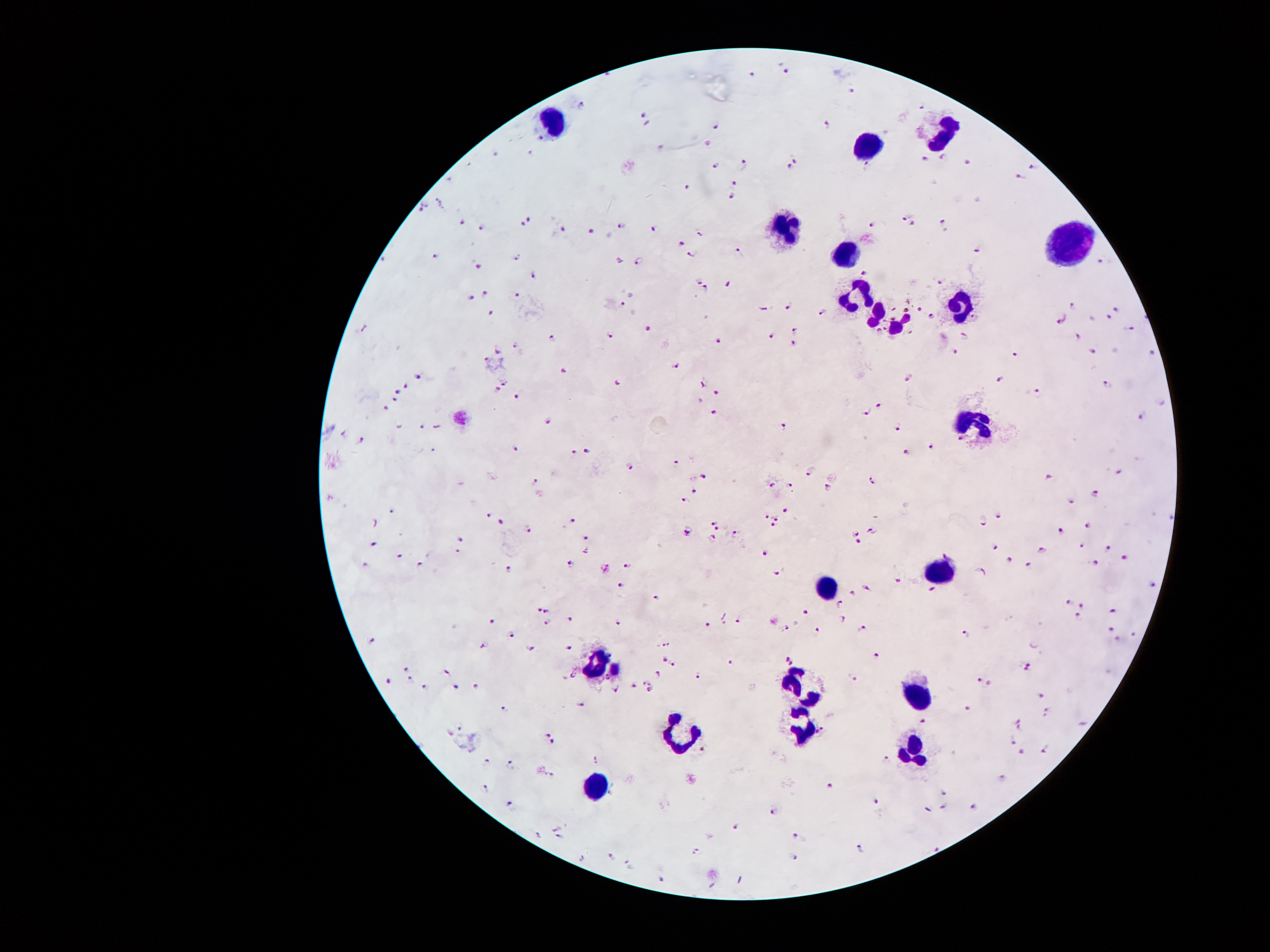

Patient malaria status: positive for Plasmodium falciparum. Single field of view. Image is 1270×952 pixels. Smartphone photograph taken through the microscope eyepiece. Giemsa stain. Thick peripheral-blood smear. 100x magnification.